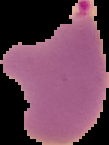 The area outside the segmented cell region is set to black. Result: Plasmodium parasites identified. From a thin blood smear. Image is 109×145 pixels.